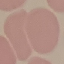

Summary:
  - Malaria status: uninfected
  - Capture: smartphone camera at the microscope eyepiece
  - Preparation: thin blood smear
  - Image type: automatically extracted cell patch, resized to 64 × 64 pixels
  - Stain: Giemsa